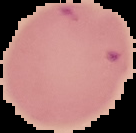
The area outside the segmented cell region is set to black. Image is 136×133 pixels. Result: Plasmodium parasites identified. From a thin blood smear.